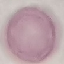

Summary:
  - Result: no malaria parasites seen
  - Capture: smartphone through the microscope eyepiece
  - Preparation: thin blood smear
  - Image type: automatically extracted cell patch, resized to 64 × 64 pixels
  - Stain: Giemsa